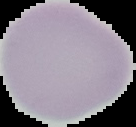

From a thin blood smear. Result: no malaria parasites seen. Image is 136×127 pixels. The area outside the segmented cell region is set to black.